Name the blood parasite species.
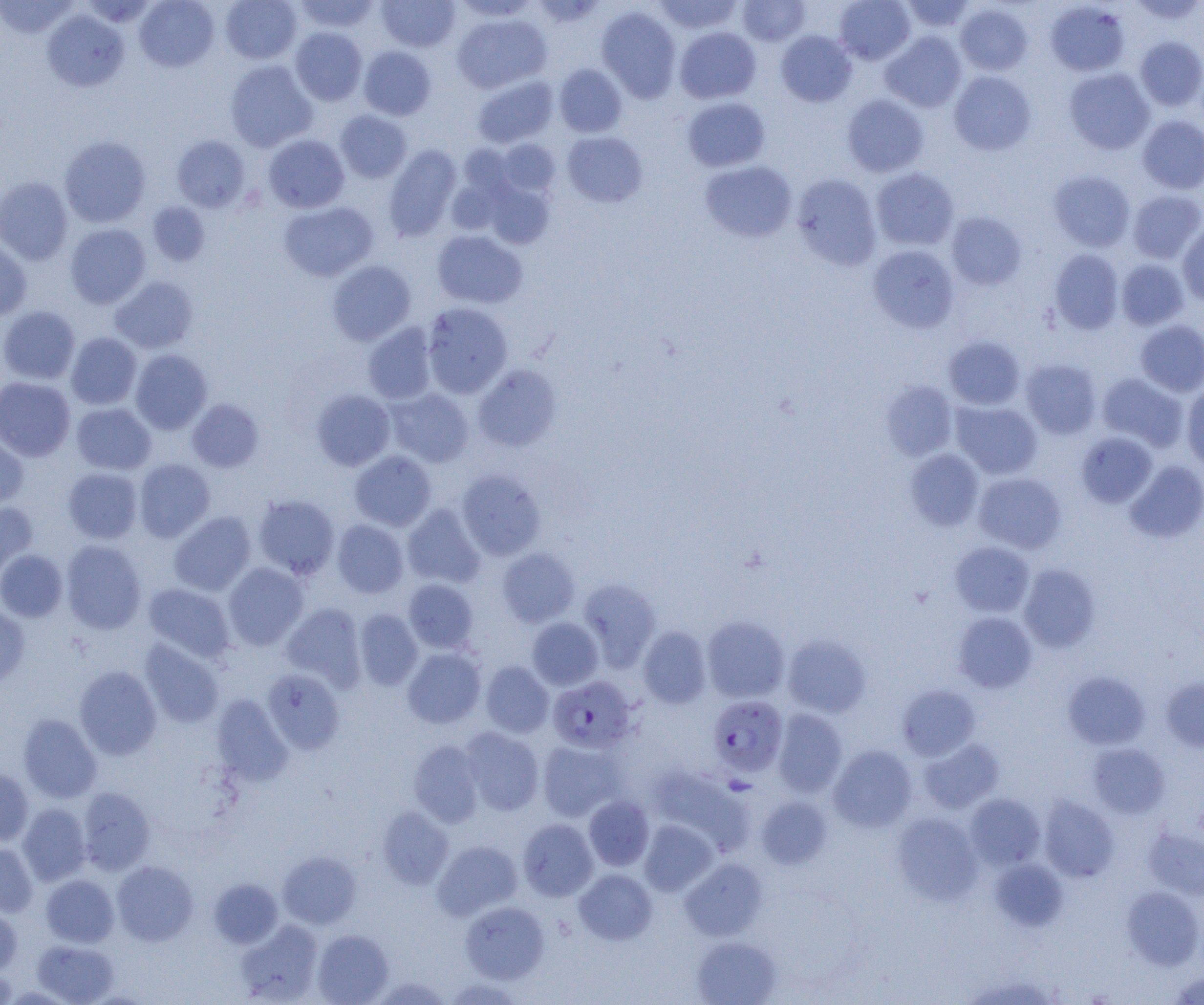
Plasmodium falciparum.

modality: light microscopy
preparation: thin blood film
plasmodium_falciparum_infected_red_blood_cell_locations: 'approximate bounding boxes as named x1/y1/x2/y2 corners in pixels: (x1=548, y1=676, x2=636, y2=753), (x1=708, y1=695, x2=788, y2=777)'
uninfected_red_blood_cell_locations: 'approximate bounding boxes as named x1/y1/x2/y2 corners in pixels: (x1=135, y1=0, x2=219, y2=72), (x1=220, y1=0, x2=302, y2=64), (x1=293, y1=0, x2=379, y2=33), (x1=452, y1=0, x2=540, y2=21), (x1=531, y1=0, x2=608, y2=29), (x1=653, y1=0, x2=743, y2=34), (x1=834, y1=0, x2=915, y2=65), (x1=900, y1=0, x2=975, y2=33), (x1=1129, y1=0, x2=1204, y2=24), (x1=0, y1=1, x2=78, y2=39), (x1=378, y1=1, x2=460, y2=52), (x1=737, y1=1, x2=811, y2=46), (x1=1045, y1=1, x2=1130, y2=76), (x1=955, y1=4, x2=1033, y2=76), (x1=596, y1=6, x2=682, y2=102), (x1=42, y1=10, x2=129, y2=92), (x1=452, y1=13, x2=551, y2=93), (x1=674, y1=26, x2=761, y2=103), (x1=290, y1=27, x2=367, y2=106), (x1=776, y1=30, x2=856, y2=107), (x1=880, y1=30, x2=967, y2=112), (x1=1135, y1=36, x2=1204, y2=110), (x1=358, y1=46, x2=436, y2=120), (x1=224, y1=60, x2=318, y2=152), (x1=554, y1=64, x2=627, y2=137), (x1=1064, y1=68, x2=1155, y2=154), (x1=949, y1=71, x2=1036, y2=155), (x1=472, y1=75, x2=558, y2=148), (x1=842, y1=94, x2=929, y2=177), (x1=682, y1=97, x2=770, y2=172), (x1=335, y1=110, x2=412, y2=183), (x1=1138, y1=116, x2=1204, y2=194), (x1=562, y1=131, x2=648, y2=207), (x1=263, y1=134, x2=349, y2=213), (x1=59, y1=136, x2=151, y2=228), (x1=172, y1=136, x2=250, y2=212), (x1=495, y1=138, x2=561, y2=197), (x1=458, y1=144, x2=516, y2=199), (x1=383, y1=145, x2=462, y2=241), (x1=700, y1=160, x2=797, y2=242), (x1=870, y1=168, x2=959, y2=250), (x1=1049, y1=170, x2=1135, y2=252), (x1=791, y1=173, x2=882, y2=270), (x1=0, y1=177, x2=73, y2=264), (x1=484, y1=180, x2=555, y2=249), (x1=1127, y1=190, x2=1204, y2=263), (x1=279, y1=201, x2=378, y2=281), (x1=147, y1=202, x2=210, y2=265), (x1=945, y1=211, x2=1026, y2=291), (x1=1177, y1=222, x2=1204, y2=307), (x1=65, y1=223, x2=151, y2=308), (x1=432, y1=230, x2=528, y2=309), (x1=0, y1=241, x2=32, y2=320), (x1=867, y1=245, x2=959, y2=333), (x1=1049, y1=249, x2=1124, y2=334), (x1=1116, y1=259, x2=1189, y2=330), (x1=327, y1=260, x2=416, y2=345), (x1=110, y1=276, x2=199, y2=353), (x1=421, y1=302, x2=514, y2=398), (x1=0, y1=305, x2=80, y2=385), (x1=1135, y1=320, x2=1204, y2=396), (x1=362, y1=322, x2=437, y2=404), (x1=66, y1=332, x2=141, y2=409), (x1=943, y1=335, x2=1025, y2=410), (x1=131, y1=349, x2=212, y2=434), (x1=1021, y1=359, x2=1101, y2=438), (x1=472, y1=364, x2=562, y2=452), (x1=1097, y1=373, x2=1187, y2=450), (x1=0, y1=377, x2=75, y2=461), (x1=881, y1=381, x2=958, y2=460), (x1=1182, y1=384, x2=1204, y2=471), (x1=385, y1=388, x2=474, y2=467), (x1=311, y1=389, x2=395, y2=471), (x1=187, y1=398, x2=264, y2=472), (x1=951, y1=401, x2=1042, y2=479), (x1=72, y1=403, x2=156, y2=475), (x1=1076, y1=432, x2=1157, y2=508), (x1=0, y1=433, x2=29, y2=510), (x1=904, y1=449, x2=984, y2=530), (x1=349, y1=450, x2=437, y2=531), (x1=134, y1=458, x2=215, y2=542), (x1=1124, y1=459, x2=1204, y2=543), (x1=63, y1=467, x2=143, y2=544), (x1=456, y1=469, x2=546, y2=560), (x1=973, y1=472, x2=1066, y2=553), (x1=253, y1=494, x2=339, y2=579), (x1=0, y1=502, x2=38, y2=579), (x1=402, y1=504, x2=486, y2=589), (x1=169, y1=511, x2=256, y2=596), (x1=332, y1=519, x2=409, y2=598), (x1=60, y1=540, x2=147, y2=634), (x1=949, y1=541, x2=1034, y2=617), (x1=497, y1=547, x2=580, y2=627), (x1=0, y1=549, x2=67, y2=622), (x1=223, y1=562, x2=308, y2=650), (x1=1019, y1=563, x2=1100, y2=652), (x1=403, y1=578, x2=478, y2=653), (x1=578, y1=578, x2=661, y2=669), (x1=143, y1=583, x2=235, y2=662), (x1=280, y1=602, x2=366, y2=690), (x1=0, y1=606, x2=30, y2=686), (x1=354, y1=609, x2=423, y2=691), (x1=953, y1=612, x2=1037, y2=693), (x1=702, y1=616, x2=789, y2=702), (x1=527, y1=617, x2=603, y2=690), (x1=638, y1=626, x2=711, y2=708), (x1=782, y1=635, x2=871, y2=717), (x1=140, y1=639, x2=224, y2=728), (x1=402, y1=647, x2=486, y2=729), (x1=480, y1=661, x2=554, y2=737), (x1=74, y1=665, x2=162, y2=760), (x1=262, y1=669, x2=345, y2=754), (x1=1063, y1=671, x2=1150, y2=749), (x1=1160, y1=675, x2=1204, y2=752), (x1=897, y1=684, x2=980, y2=760), (x1=212, y1=694, x2=293, y2=786), (x1=772, y1=709, x2=848, y2=796), (x1=18, y1=713, x2=101, y2=803), (x1=460, y1=727, x2=544, y2=816), (x1=919, y1=738, x2=1004, y2=814), (x1=409, y1=739, x2=485, y2=827), (x1=537, y1=740, x2=626, y2=821), (x1=1087, y1=742, x2=1169, y2=818), (x1=828, y1=745, x2=916, y2=832), (x1=649, y1=765, x2=752, y2=853), (x1=0, y1=767, x2=34, y2=846), (x1=77, y1=787, x2=155, y2=875), (x1=964, y1=793, x2=1045, y2=870), (x1=584, y1=795, x2=654, y2=870), (x1=756, y1=795, x2=833, y2=869), (x1=1038, y1=796, x2=1119, y2=882), (x1=17, y1=803, x2=91, y2=886), (x1=376, y1=807, x2=454, y2=890), (x1=892, y1=812, x2=983, y2=904), (x1=518, y1=818, x2=598, y2=901), (x1=639, y1=819, x2=717, y2=895), (x1=1143, y1=826, x2=1204, y2=899), (x1=433, y1=840, x2=522, y2=920), (x1=0, y1=841, x2=38, y2=916), (x1=278, y1=850, x2=361, y2=929), (x1=681, y1=858, x2=766, y2=941), (x1=989, y1=858, x2=1068, y2=931), (x1=111, y1=860, x2=198, y2=945), (x1=574, y1=869, x2=657, y2=944), (x1=40, y1=874, x2=119, y2=947), (x1=208, y1=878, x2=283, y2=948), (x1=1122, y1=886, x2=1203, y2=969), (x1=461, y1=901, x2=549, y2=984), (x1=0, y1=905, x2=21, y2=975), (x1=235, y1=920, x2=323, y2=1004), (x1=312, y1=929, x2=394, y2=1004), (x1=692, y1=936, x2=781, y2=1005), (x1=32, y1=940, x2=118, y2=1004), (x1=0, y1=969, x2=16, y2=1003), (x1=1169, y1=971, x2=1204, y2=1004), (x1=444, y1=977, x2=524, y2=1004)'
field_of_view: single
image_size: 1204×1005 pixels
magnification: 1000x